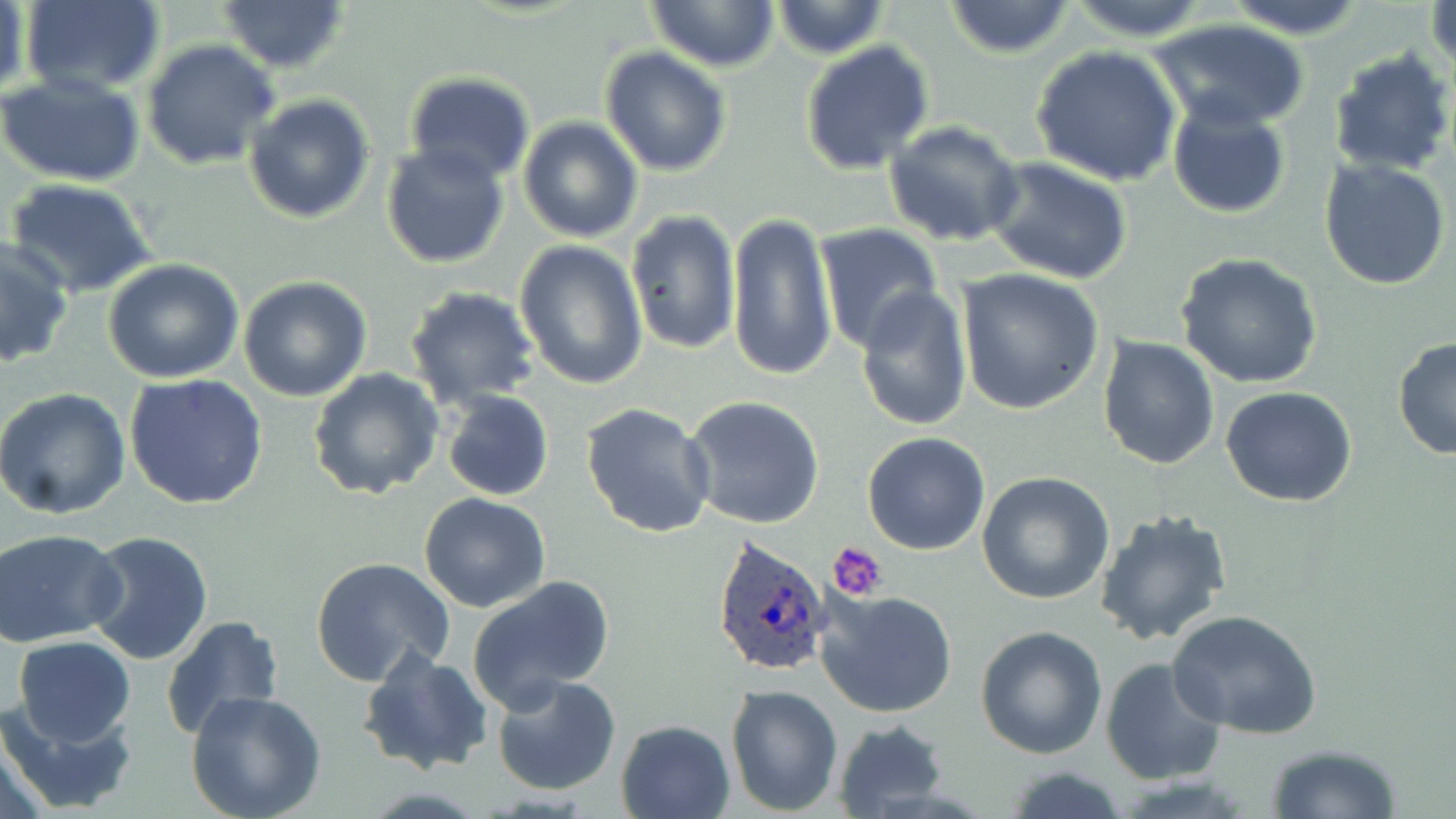

slide-level diagnosis = Plasmodium ovale
field of view = one of a larger specimen
uninfected red blood cell locations = approximate bounding boxes as (x1,y1)-(x2,y2) corner pairs in pixels: (19,0)-(166,96), (217,0)-(351,73), (942,0)-(1078,59), (1219,0)-(1371,37), (1426,0)-(1455,80), (646,1)-(779,72), (771,1)-(889,59), (1062,1)-(1213,41), (2,2)-(33,106), (1148,18)-(1311,132), (142,40)-(281,171), (800,41)-(935,176), (1030,45)-(1182,187), (599,46)-(731,176), (1327,49)-(1455,178), (403,72)-(536,188), (0,73)-(145,187), (243,93)-(375,224), (1166,99)-(1291,217), (518,116)-(644,243), (884,120)-(1025,248), (380,142)-(510,267), (985,156)-(1134,285), (1318,156)-(1453,290), (4,177)-(159,298), (625,210)-(741,358), (726,210)-(835,382), (816,224)-(945,354), (0,239)-(73,367), (513,240)-(648,390), (1177,254)-(1323,391), (102,260)-(245,384), (956,270)-(1106,415), (239,275)-(372,402), (403,285)-(541,409), (855,285)-(973,431), (1097,335)-(1220,470), (1392,337)-(1455,460), (308,368)-(443,502), (125,373)-(268,509), (1220,385)-(1357,507), (0,388)-(132,519), (440,388)-(554,501), (684,395)-(825,530), (581,403)-(717,539), (862,432)-(991,556), (976,473)-(1116,606), (419,492)-(550,612), (1093,507)-(1233,648), (1,529)-(127,646), (83,529)-(216,666), (311,556)-(456,688), (467,576)-(615,709), (816,588)-(958,719), (1166,610)-(1322,738), (160,615)-(286,741), (977,624)-(1108,758), (13,637)-(137,747), (358,647)-(492,776), (1099,658)-(1226,786), (489,671)-(622,795), (725,683)-(845,815), (185,691)-(327,819), (0,694)-(140,816), (615,718)-(737,819), (832,720)-(951,816), (0,721)-(55,819), (1265,742)-(1402,818), (1000,763)-(1133,819)
platelet locations = approximate bounding boxes as (x1,y1)-(x2,y2) corner pairs in pixels: (829,542)-(890,602)
image size = 1456×819 pixels
magnification = 1000x
Plasmodium ovale-infected red blood cell locations = approximate bounding boxes as (x1,y1)-(x2,y2) corner pairs in pixels: (710,535)-(836,679)
preparation = thin blood smear
stain = May-Grünwald-Giemsa
modality = light microscopy